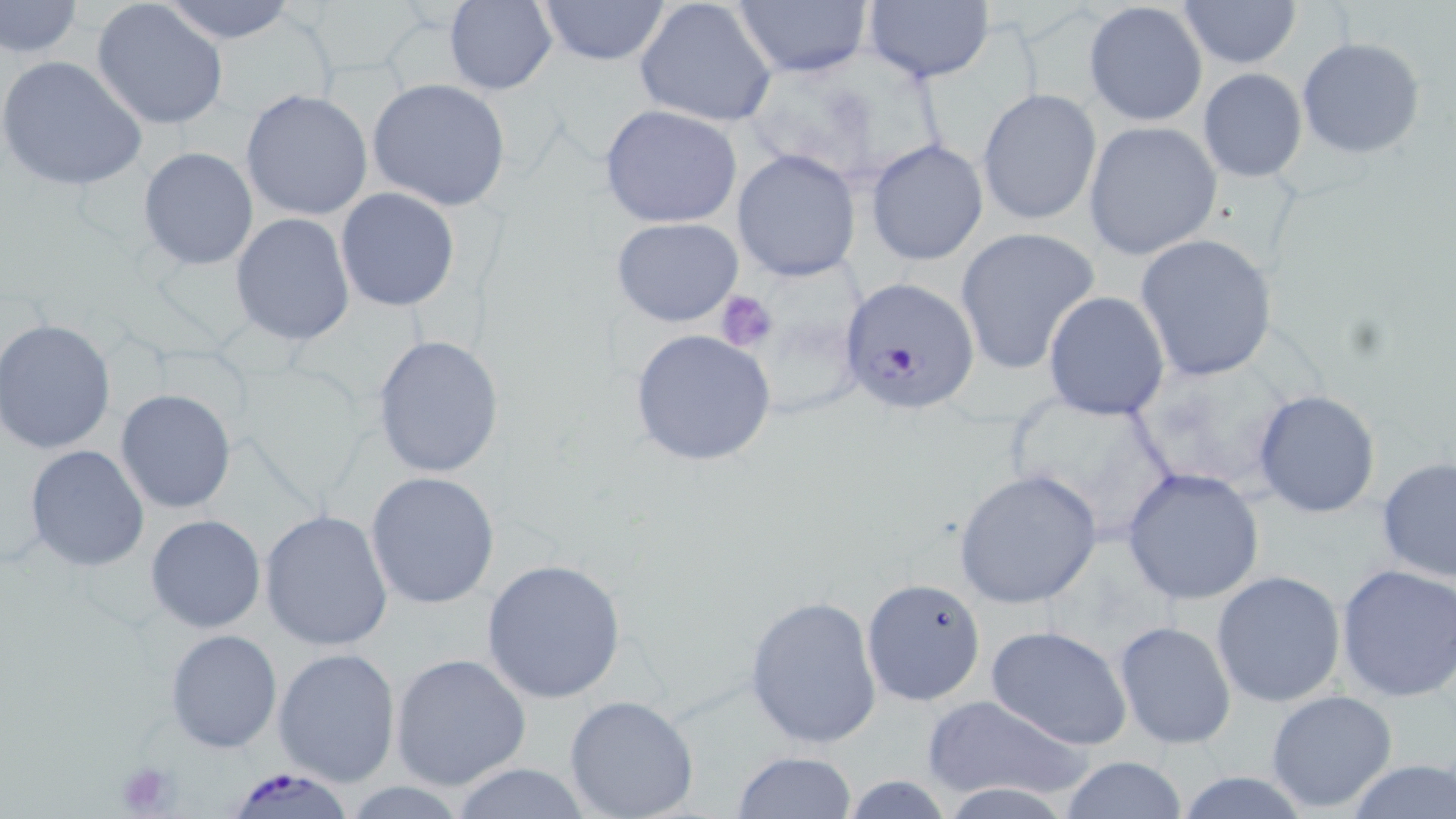

Approximate bounding boxes as [x1, y1, x2, y2] in pixels. Uninfected red blood cell locations: [1, 0, 83, 59], [158, 0, 301, 44], [532, 0, 674, 68], [634, 0, 778, 128], [730, 0, 872, 77], [1176, 0, 1302, 68], [443, 1, 557, 95], [90, 2, 230, 131], [863, 2, 995, 84], [1085, 2, 1208, 127], [1297, 36, 1426, 159], [0, 53, 148, 191], [1197, 67, 1309, 181], [367, 78, 512, 213], [978, 88, 1102, 226], [240, 89, 372, 221], [599, 103, 744, 228], [1084, 121, 1223, 260], [865, 138, 990, 267], [138, 146, 259, 271], [732, 148, 861, 281], [335, 187, 461, 312], [229, 213, 355, 346], [611, 217, 744, 326], [953, 227, 1100, 375], [1135, 234, 1280, 383], [1042, 291, 1170, 421], [1, 319, 116, 454], [629, 328, 777, 468], [371, 334, 504, 478], [1131, 353, 1301, 492], [1000, 387, 1180, 546], [115, 389, 237, 514], [1252, 389, 1383, 519], [25, 444, 149, 572], [1376, 456, 1456, 586], [1120, 467, 1265, 608], [953, 468, 1104, 611], [366, 471, 500, 610], [260, 510, 394, 652], [145, 514, 267, 635], [480, 559, 629, 704], [1335, 563, 1456, 702], [1211, 571, 1347, 708], [861, 576, 988, 707], [743, 595, 882, 749], [1112, 621, 1236, 751], [986, 625, 1134, 750], [164, 628, 281, 753], [271, 647, 401, 785], [390, 654, 532, 791], [1265, 689, 1400, 813], [563, 694, 700, 819], [921, 694, 1095, 804], [731, 750, 858, 818], [1056, 756, 1191, 818], [1344, 758, 1456, 819], [445, 762, 596, 819]. Plasmodium falciparum-infected red blood cell locations: [839, 278, 977, 413], [224, 766, 358, 819]. Platelet locations: [713, 290, 778, 353], [112, 758, 182, 819]. Slide-level diagnosis: Plasmodium falciparum. Single field of view. Light microscopy. May-Grünwald-Giemsa stain. Image is 1456×819 pixels. Captured at 1000x magnification. Thin blood smear.